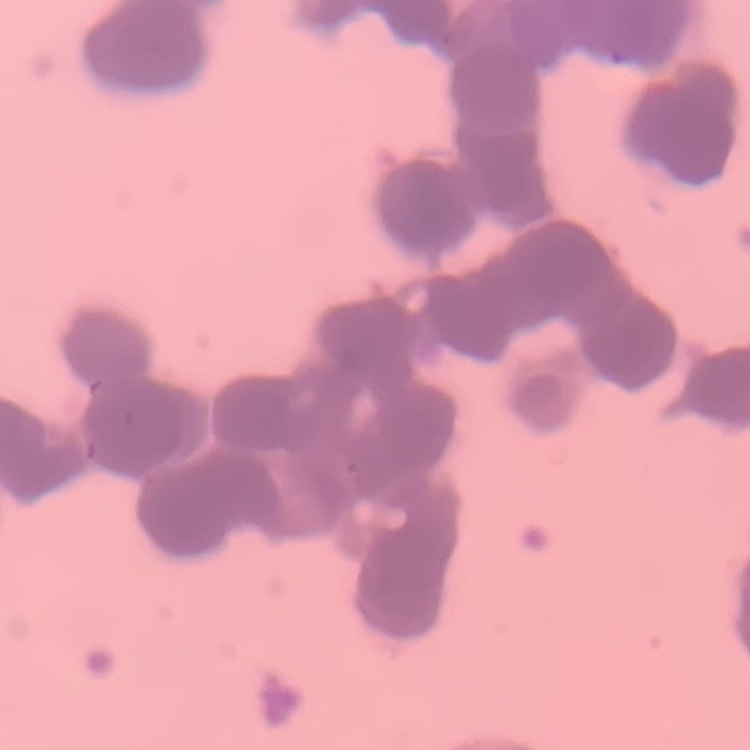

red blood cell morphology = rouleaux formation
stain = Field's or Giemsa
preparation = thin blood smear
image type = square crop of a larger photomicrograph